Assess this cell for malaria.
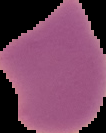

It is parasitized.

image type = segmented cell region on a black background
preparation = thin blood film
image size = 106×133 pixels